Comment on the morphology of the red blood cells.
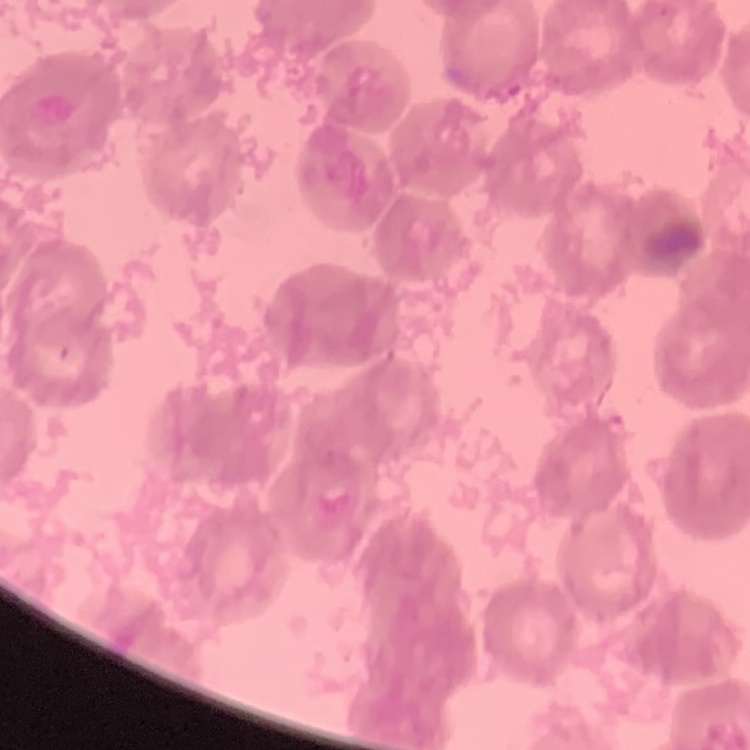

Rouleaux formation.

Field's or Giemsa stain. Square crop of a larger photomicrograph. Thin blood film.